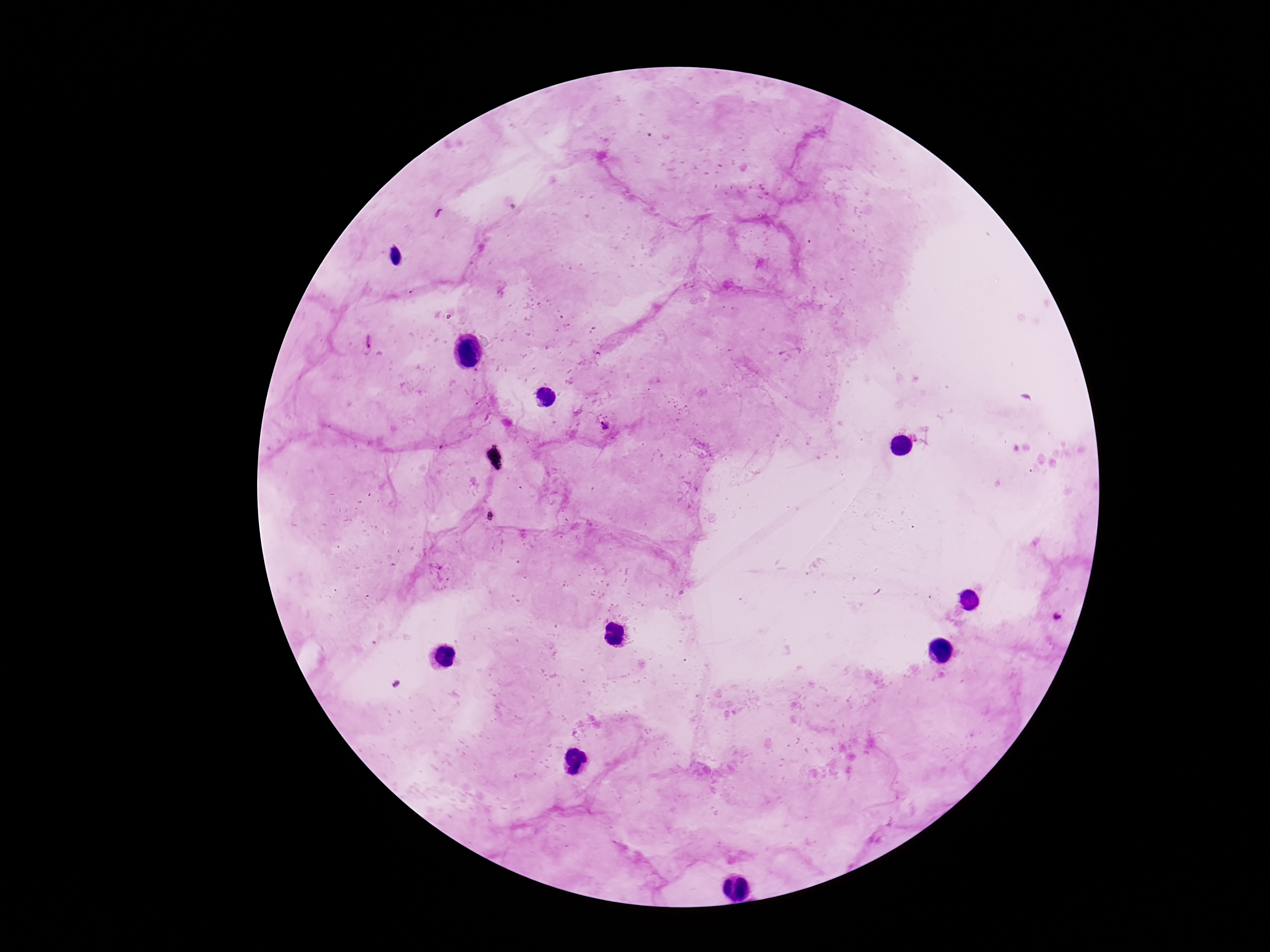

Approximate centers as [x, y] in pixels.
Summary:
  - Plasmodium parasite locations: [368, 341], [604, 426], [1059, 617]
  - Image size: 1270×952 pixels
  - Field of view: single
  - Patient malaria status: infected
  - Stain: Giemsa
  - Preparation: thick peripheral-blood smear
  - Capture: smartphone camera through the microscope eyepiece
  - Magnification: 100x